Classify this cell by malaria status.
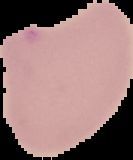
Uninfected.

From a thin blood smear. Image is 133×160 pixels. The area outside the segmented cell region is set to black.